Assess for malaria.
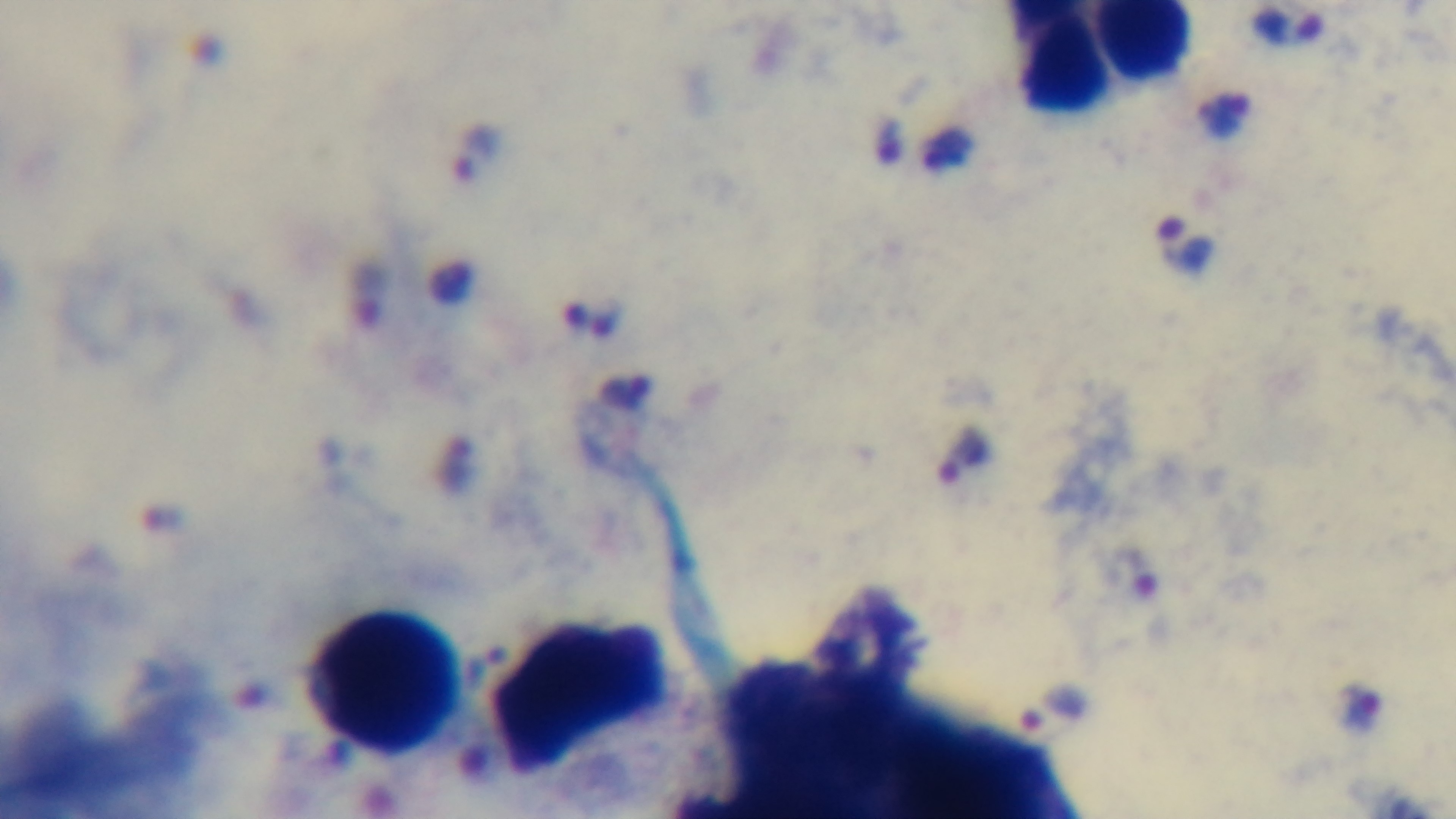
Infected.

Oil-immersion objective, 100x. Light microscopy. Mounted 4K digital camera. Preparation: thick. Single field of view. Giemsa-stained.